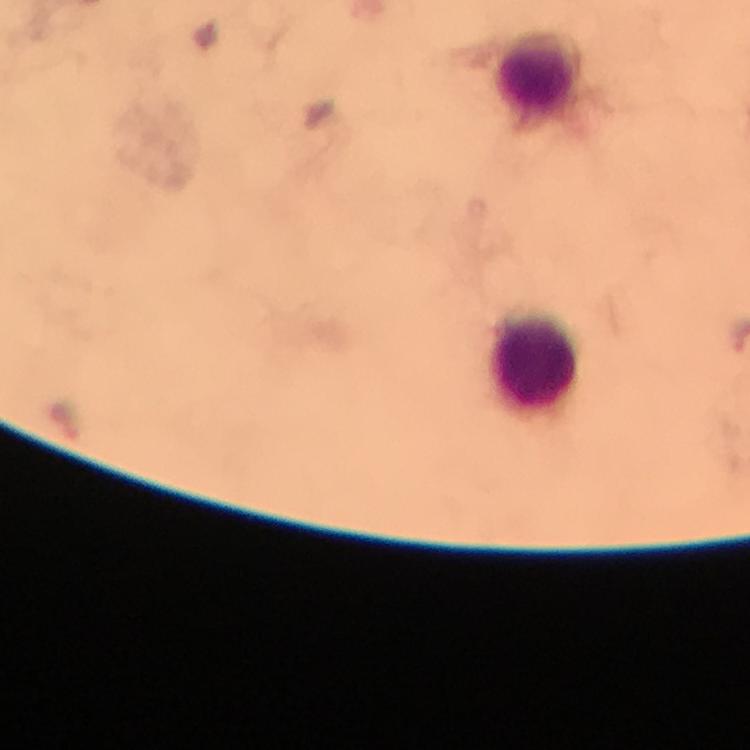
Approximate object centers, in pixels from the top-left corner. Leukocyte locations: (x=535, y=73). From a malaria diagnostic workup. Giemsa-stained preparation. Thick blood film. Immersion oil was used. Malaria parasites: none detected. Image is 750×750 pixels. A crop from one field of view. Smartphone photograph taken through a microscope. 100x magnification.